Outline each blood parasite and name the species.
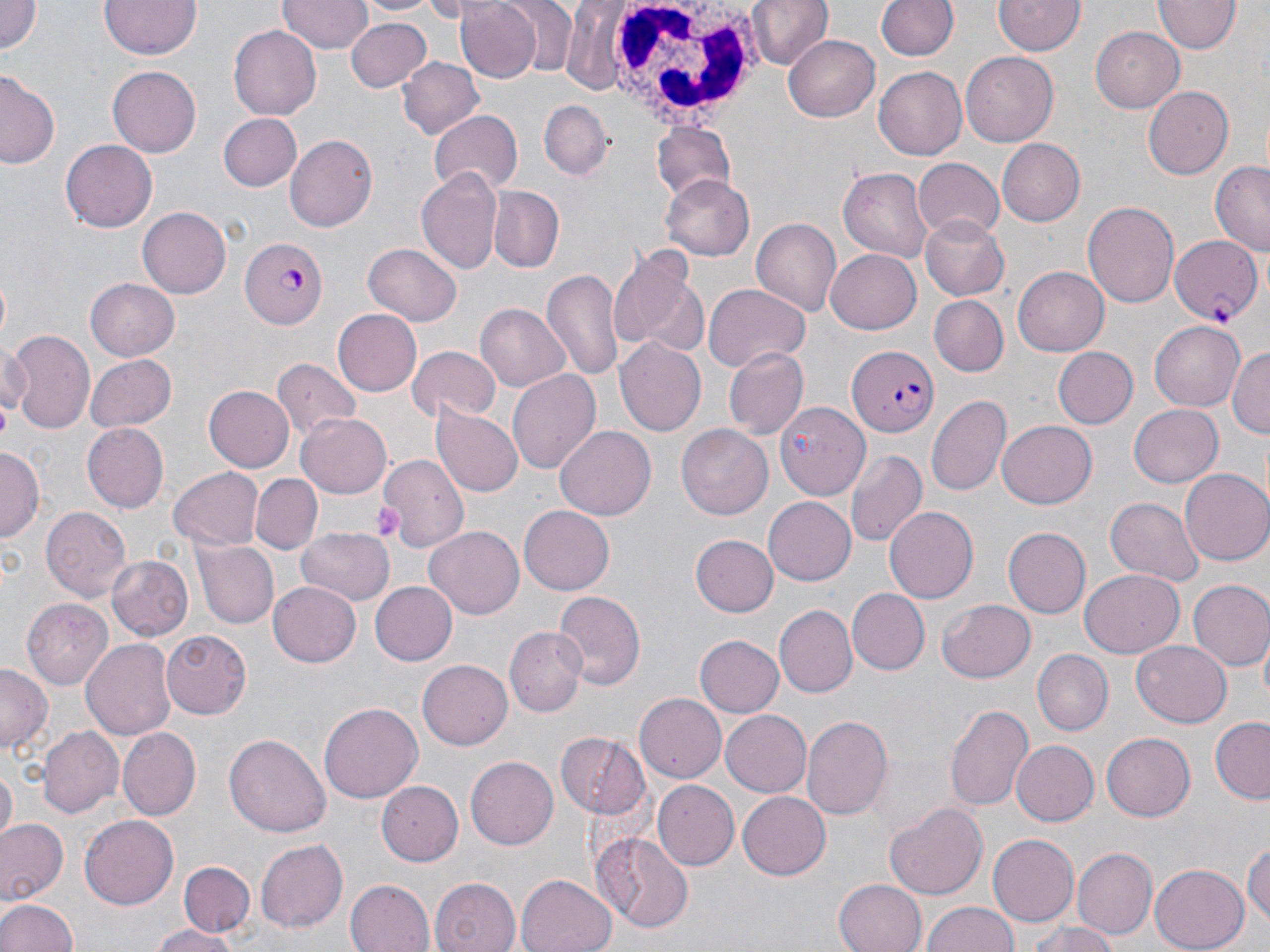

Approximate bounding boxes as (x1, y1, x2, y2) in pixels.
Plasmodium falciparum-infected red blood cells: (1170, 236, 1261, 325), (239, 237, 326, 330), (847, 346, 939, 437).
No Plasmodium ovale, Plasmodium malariae, Plasmodium vivax, Babesia divergens, or Trypanosoma brucei observed.

Uninfected red blood cell locations: (0, 0, 42, 56), (98, 0, 203, 61), (357, 0, 443, 18), (496, 0, 581, 77), (743, 0, 831, 72), (873, 0, 960, 64), (1155, 0, 1239, 54), (277, 1, 370, 55), (456, 1, 543, 83), (995, 1, 1084, 58), (345, 18, 432, 92), (229, 25, 322, 120), (1091, 27, 1184, 113), (785, 33, 880, 119), (962, 53, 1058, 147), (398, 55, 484, 138), (106, 63, 201, 155), (415, 69, 512, 167), (875, 69, 967, 159), (0, 70, 62, 171), (1143, 84, 1233, 180), (538, 99, 615, 179), (428, 111, 523, 196), (217, 113, 302, 191), (650, 124, 736, 205), (285, 134, 375, 233), (60, 138, 158, 233), (996, 138, 1084, 227), (912, 159, 1005, 241), (1208, 161, 1270, 257), (838, 167, 935, 261), (417, 168, 502, 273), (661, 175, 754, 259), (491, 186, 563, 271), (1083, 201, 1180, 308), (137, 204, 230, 296), (920, 215, 1009, 301), (752, 218, 842, 317), (361, 242, 461, 326), (610, 242, 708, 359), (826, 248, 924, 333), (1012, 265, 1109, 356), (543, 268, 626, 385), (85, 277, 181, 360), (704, 285, 810, 372), (930, 296, 1008, 375), (475, 305, 570, 392), (332, 308, 422, 396), (1150, 318, 1246, 408), (6, 330, 95, 431), (0, 337, 28, 418), (613, 339, 706, 437), (1229, 345, 1269, 440), (1053, 346, 1137, 428), (724, 347, 809, 439), (407, 348, 502, 424), (85, 354, 177, 433), (272, 358, 361, 439), (509, 370, 600, 475), (202, 385, 293, 473), (928, 393, 1011, 497), (433, 402, 525, 496), (774, 403, 869, 500), (1129, 403, 1223, 487), (296, 413, 393, 498), (997, 421, 1097, 508), (81, 422, 167, 514), (555, 425, 656, 522), (676, 425, 773, 520), (377, 437, 479, 549), (0, 448, 43, 541), (844, 450, 926, 547), (169, 466, 262, 550), (1180, 469, 1270, 566), (252, 474, 321, 554), (1105, 497, 1203, 586), (764, 499, 856, 584), (518, 504, 614, 594), (41, 506, 132, 604), (883, 507, 977, 603), (1000, 525, 1091, 620), (424, 526, 525, 617), (295, 528, 392, 606), (692, 535, 777, 616), (194, 539, 279, 628), (106, 555, 192, 642), (1080, 569, 1184, 657), (370, 580, 456, 665), (1187, 580, 1270, 672), (269, 582, 361, 667), (848, 588, 929, 674), (555, 589, 649, 689), (939, 597, 1036, 684), (23, 598, 112, 688), (775, 605, 857, 696), (506, 627, 584, 714), (160, 630, 251, 717), (693, 635, 784, 718), (82, 637, 179, 740), (1133, 638, 1231, 723), (1031, 649, 1113, 736), (419, 661, 513, 749), (0, 665, 50, 756), (635, 691, 729, 781), (319, 702, 423, 803), (946, 703, 1034, 814), (721, 710, 812, 797), (802, 715, 893, 822), (1209, 719, 1269, 802), (41, 726, 124, 817), (119, 729, 200, 818), (1102, 730, 1195, 819), (556, 731, 650, 816), (226, 734, 330, 839), (1010, 740, 1099, 826), (466, 755, 559, 850), (2, 770, 17, 840), (378, 778, 464, 863), (651, 780, 738, 869), (737, 790, 831, 879), (886, 801, 987, 898), (81, 813, 179, 910), (0, 820, 66, 905), (594, 833, 693, 934), (990, 833, 1080, 926), (256, 838, 348, 932), (1244, 839, 1269, 932), (1075, 848, 1155, 943), (179, 859, 254, 938), (1151, 862, 1249, 951), (515, 874, 617, 952), (429, 875, 521, 952), (834, 877, 928, 952), (344, 879, 434, 952), (0, 896, 80, 952), (920, 902, 1021, 952), (1026, 919, 1117, 952), (149, 925, 242, 952). White blood cell locations: (599, 0, 766, 124). Platelet locations: (371, 505, 403, 540). Slide-level diagnosis: Plasmodium falciparum. Captured at 1000x magnification. Optical microscopy. One field of a larger specimen. Thin blood smear. Image is 1270×952 pixels. May-Grünwald-Giemsa stain.